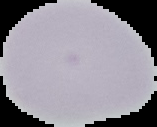

Result: no Plasmodium parasites seen. From a thin blood film. Image is 157×127 pixels. Segmented cell region on a black background.